Identify the blood parasite species.
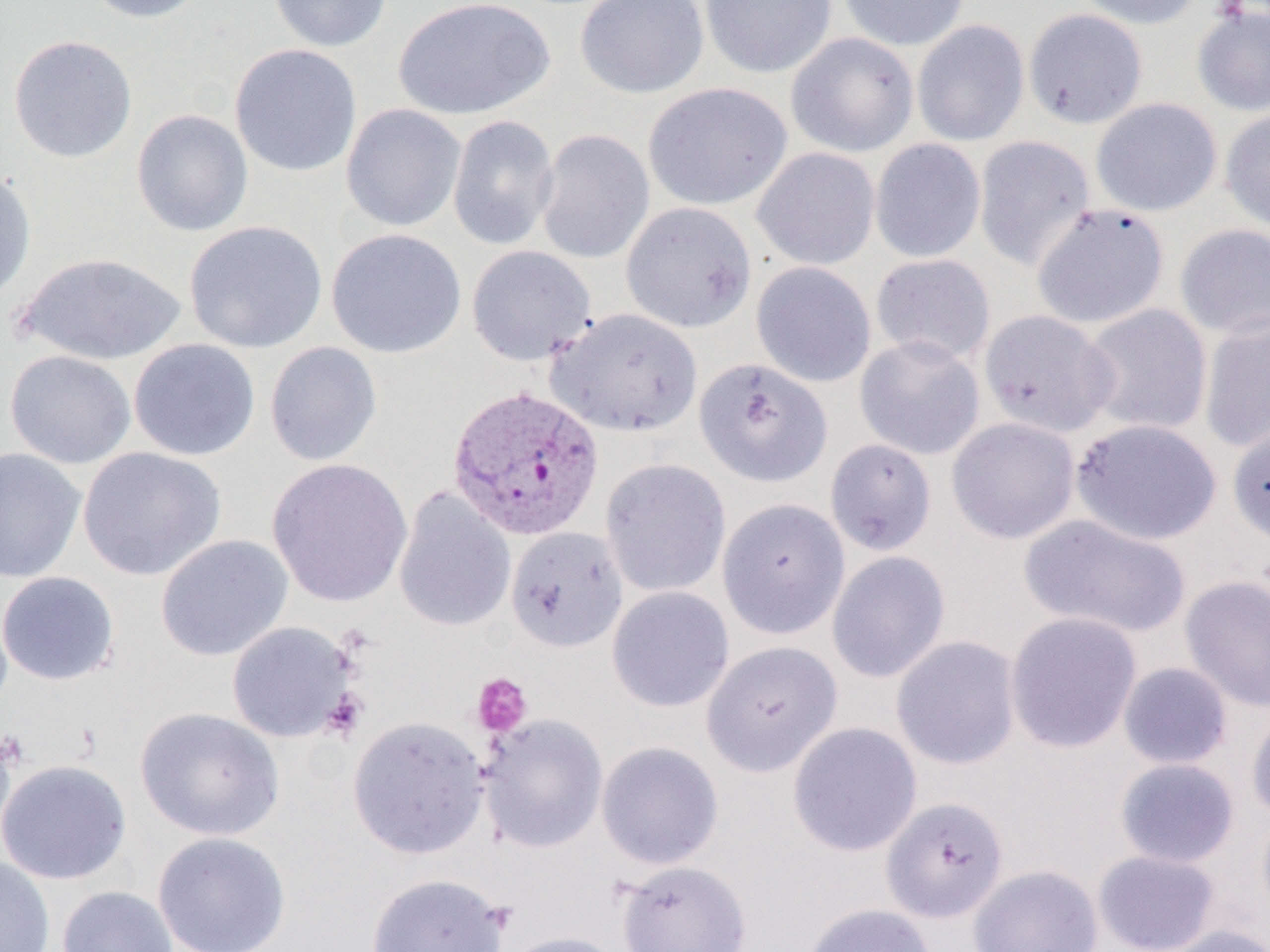

Plasmodium vivax.

Approximate bounding boxes as [x1, y1, x2, y2] in pixels. Uninfected red blood cell locations: [80, 0, 211, 23], [269, 0, 393, 53], [392, 0, 556, 121], [575, 0, 709, 99], [700, 0, 837, 79], [838, 0, 969, 51], [1073, 0, 1204, 30], [1191, 4, 1270, 118], [1023, 9, 1148, 128], [912, 20, 1029, 146], [785, 32, 919, 157], [8, 34, 137, 162], [229, 43, 362, 178], [643, 82, 792, 211], [1090, 97, 1222, 216], [340, 104, 466, 232], [1220, 107, 1270, 234], [131, 108, 253, 237], [447, 115, 559, 251], [535, 128, 655, 264], [973, 135, 1096, 270], [869, 138, 986, 263], [751, 147, 880, 270], [0, 168, 36, 305], [621, 201, 757, 333], [1032, 204, 1170, 330], [184, 220, 328, 354], [1174, 224, 1270, 340], [326, 228, 467, 359], [466, 245, 596, 366], [16, 251, 187, 366], [870, 253, 996, 365], [751, 261, 876, 387], [1080, 304, 1213, 436], [546, 308, 703, 437], [979, 309, 1117, 438], [1198, 312, 1270, 452], [854, 335, 985, 460], [129, 339, 261, 461], [264, 341, 382, 467], [4, 349, 136, 469], [694, 357, 832, 488], [946, 417, 1080, 544], [1071, 418, 1222, 545], [1227, 421, 1270, 546], [824, 438, 937, 556], [77, 446, 226, 581], [0, 447, 86, 583], [267, 458, 413, 608], [600, 458, 731, 598], [393, 487, 516, 633], [717, 498, 850, 639], [1018, 513, 1192, 639], [505, 526, 628, 652], [156, 534, 293, 661], [826, 550, 951, 683], [0, 571, 120, 686], [1179, 574, 1270, 713], [606, 586, 735, 713], [1004, 612, 1143, 754], [226, 621, 357, 743], [891, 635, 1022, 770], [701, 640, 842, 776], [1118, 662, 1233, 770], [1246, 705, 1270, 822], [135, 706, 285, 841], [478, 713, 608, 853], [347, 716, 490, 859], [787, 721, 922, 857], [0, 722, 17, 852], [596, 740, 724, 869], [1114, 757, 1240, 868], [0, 759, 132, 885], [881, 795, 1009, 924], [1256, 807, 1270, 926], [152, 831, 292, 952], [1092, 849, 1221, 952], [0, 856, 55, 952], [616, 859, 751, 952], [968, 864, 1103, 952], [365, 872, 511, 952], [56, 886, 178, 952], [802, 902, 938, 952], [1158, 924, 1270, 952], [498, 930, 630, 952]. Plasmodium vivax-infected red blood cell locations: [446, 385, 606, 541]. Platelet locations: [471, 673, 533, 738], [320, 689, 367, 741]. 1000x magnification. Light microscopy. Thin blood smear. One field of a larger specimen. Image is 1270×952 pixels.